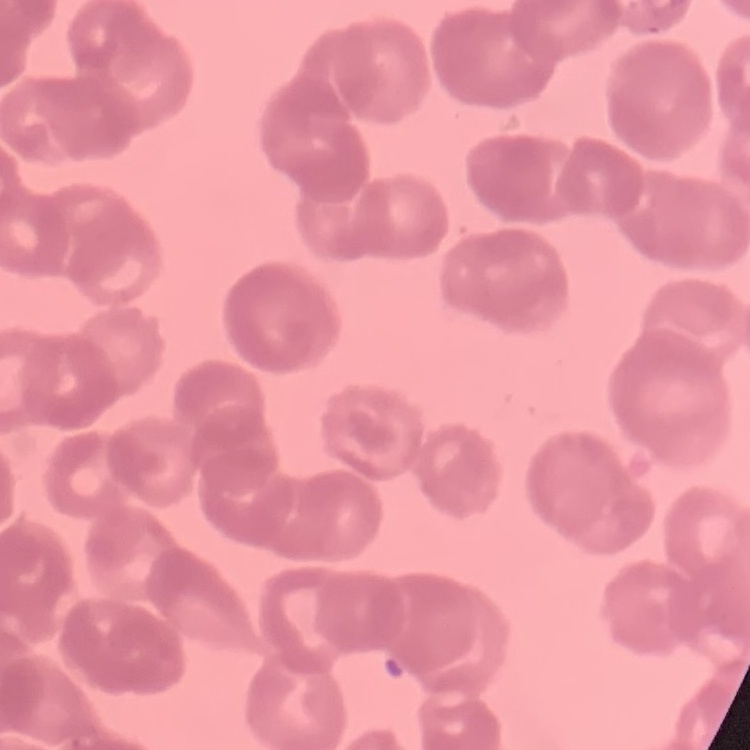

Summary:
  - Erythrocyte morphology: rouleaux formation
  - Image type: square crop of a larger photomicrograph
  - Preparation: thin blood smear
  - Stain: Field's or Giemsa